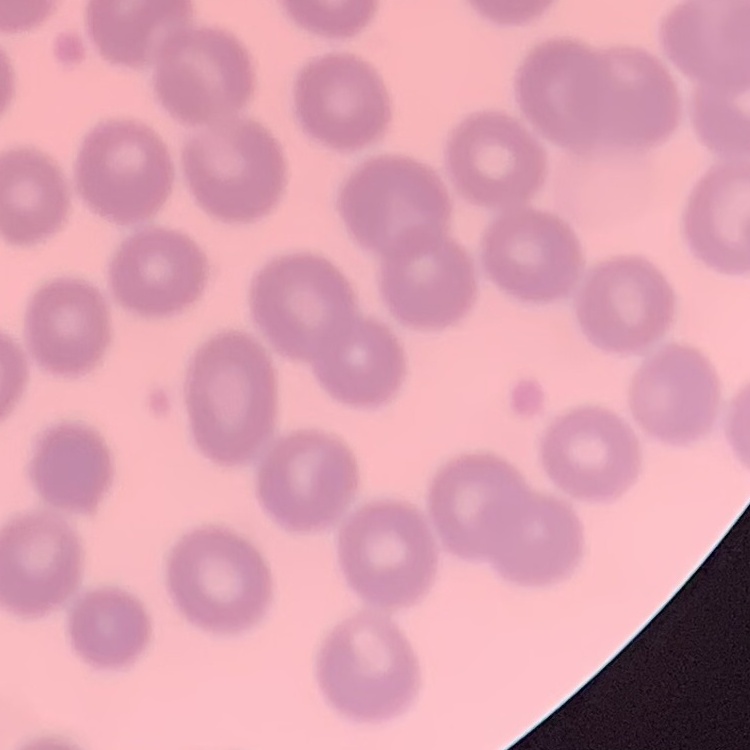
{
  "red_blood_cell_morphology": "no rouleaux formation",
  "stain": "Field's or Giemsa",
  "preparation": "thin blood smear",
  "image_type": "one tile cut from a larger photomicrograph"
}